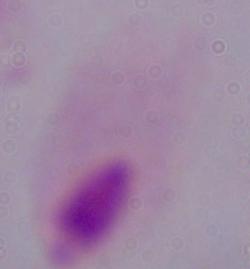
identification = trichomonad
modality = micrograph
magnification = 1000x